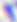 400x magnification. Micrograph. Toxoplasma gondii is shown.